Report the malaria status of this cell.
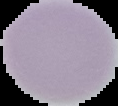

It is uninfected.

Image is 118×106 pixels. The area outside the segmented cell region is set to black. From a thin blood film.